Identify the parasite.
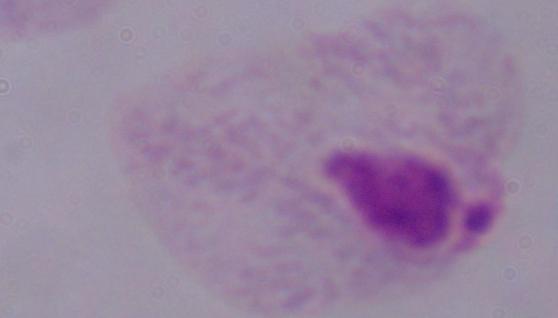

A trichomonad.

Micrograph. Captured at 1000x magnification.